Comment on the morphology of the red blood cells.
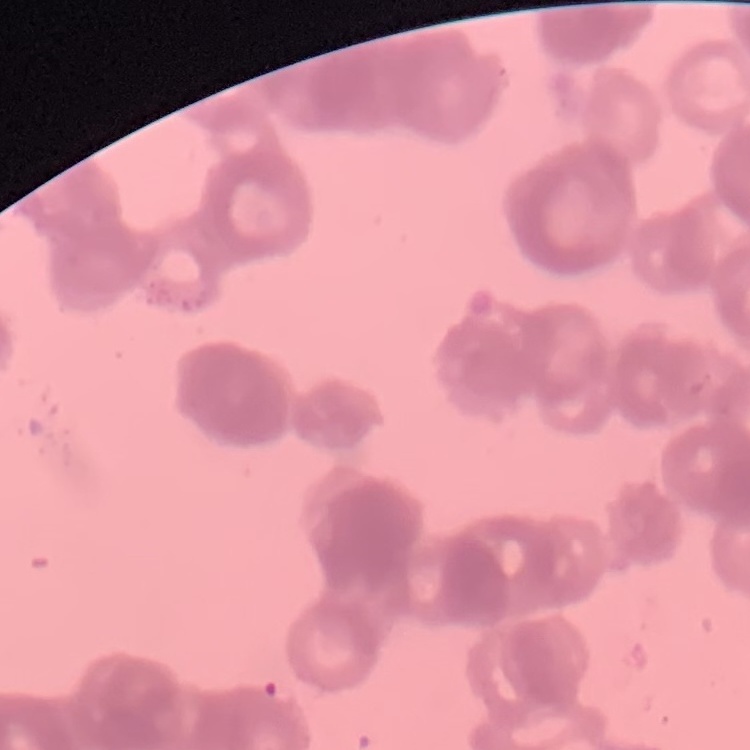

Rouleaux formation.

Square crop of a larger photomicrograph. Thin blood film. Stained with either Field's or Giemsa.